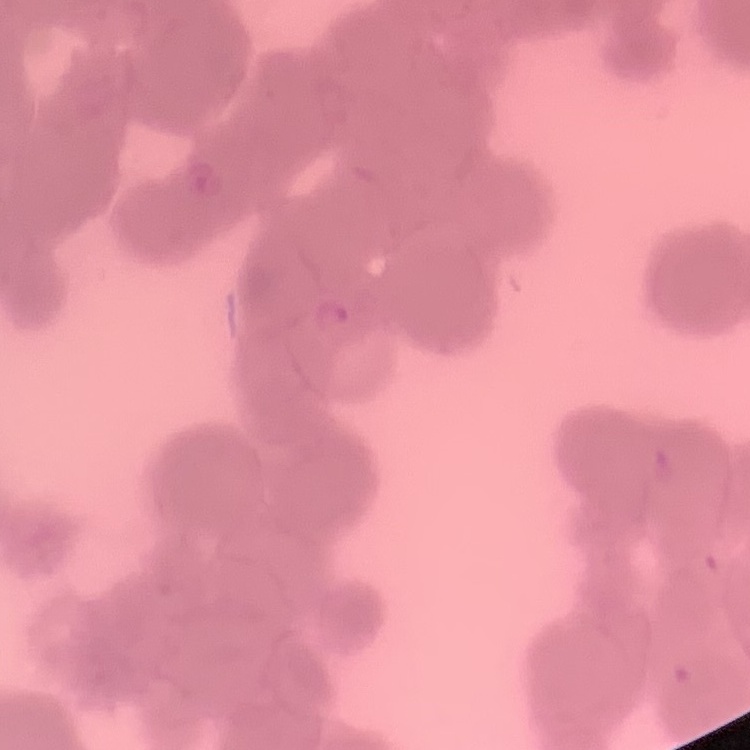
Summary:
  - Erythrocyte morphology: rouleaux formation
  - Image type: one tile cut from a larger photomicrograph
  - Stain: Field's or Giemsa
  - Preparation: thin blood smear